Comment on the morphology of the erythrocytes.
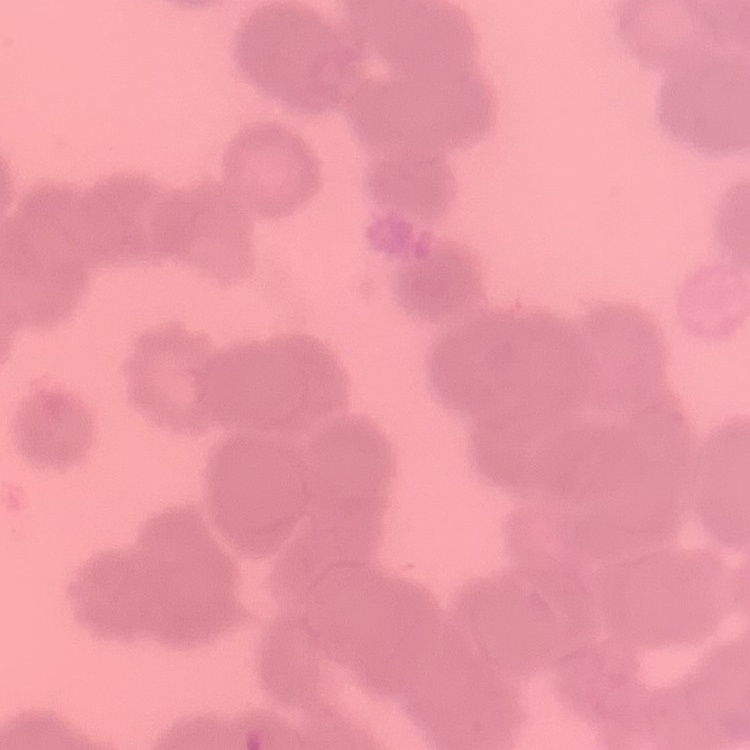

They show rouleaux formation.

Field's or Giemsa stain. One tile cut from a larger photomicrograph. Thin blood film.